State which parasite is depicted.
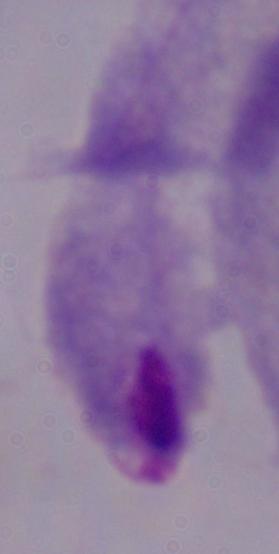

A trichomonad.

Summary:
  - Modality: micrograph
  - Magnification: 1000x